Describe the morphology of the erythrocytes.
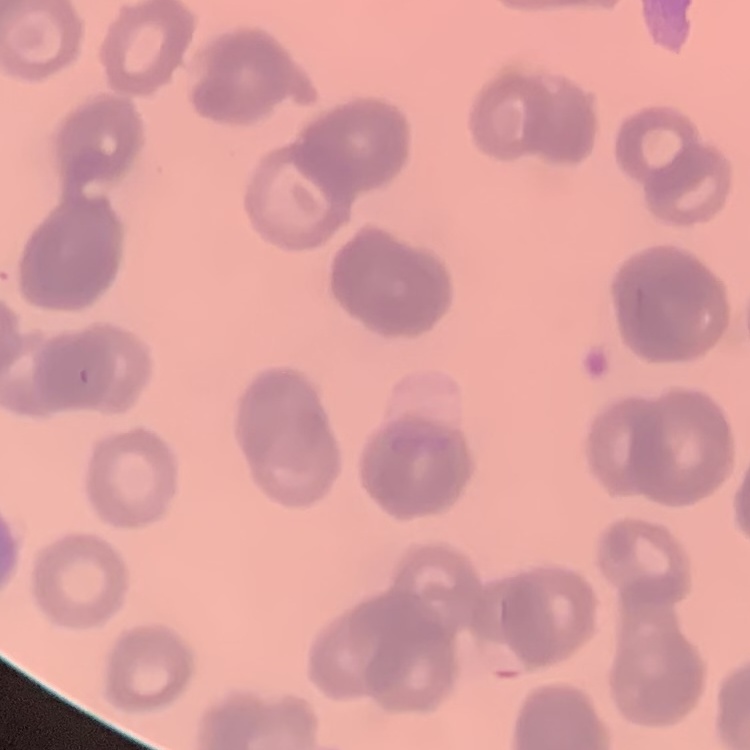
They show rouleaux formation.

Thin peripheral smear. Field's or Giemsa stain. One tile cut from a larger photomicrograph.